Assess the morphology of the red blood cells.
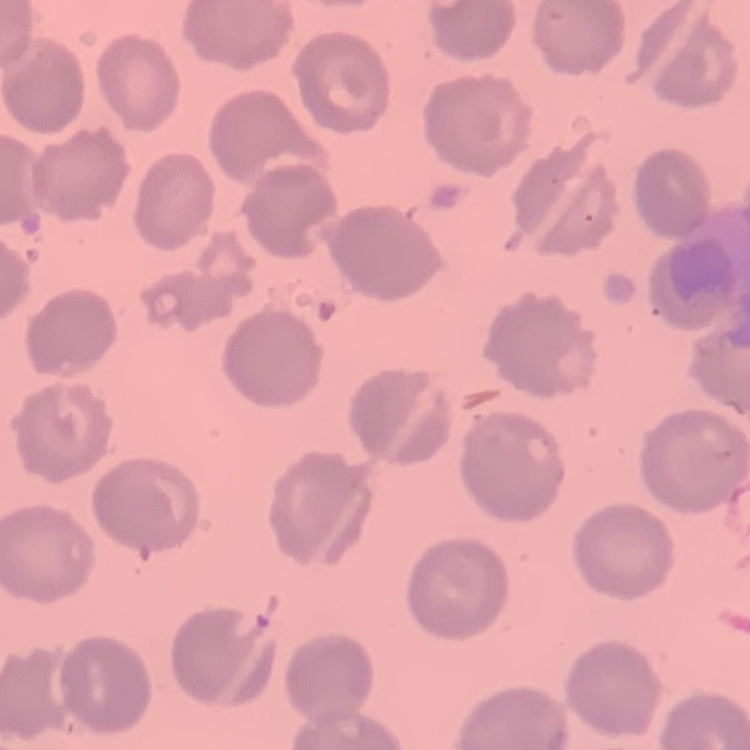
No rouleaux formation.

image_type: square crop of a larger photomicrograph
stain: Field's or Giemsa
preparation: thin blood film